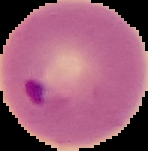

image_size: 148×151 pixels
malaria_status: parasitized
image_type: cell region segmented out of the field of view; surrounding area masked to black
preparation: thin blood film